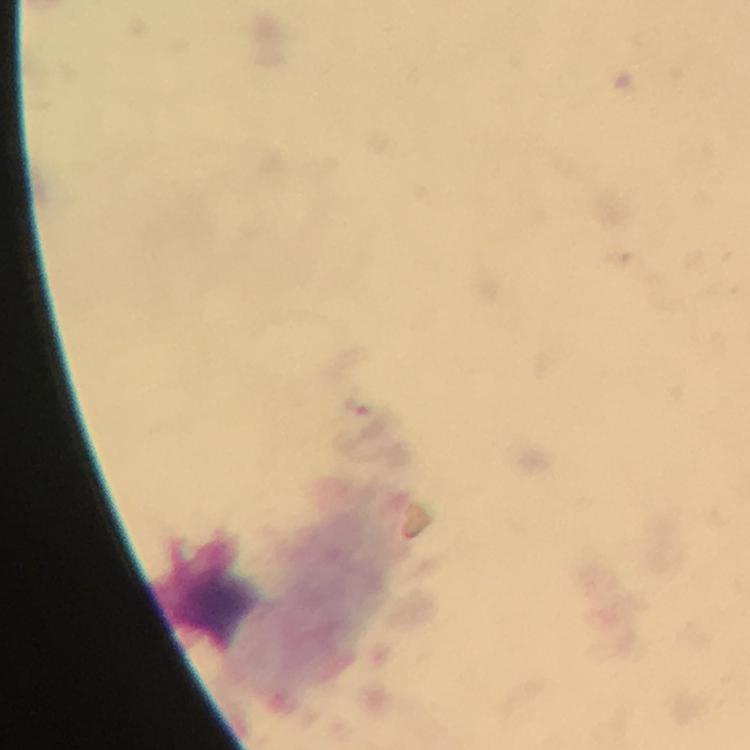

Approximate centers as {x, y} in pixels.
Summary:
  - Leukocyte locations: {214, 586}
  - Stain: Giemsa
  - Preparation: thick smear
  - Malaria parasites: none seen
  - Capture: smartphone camera through the microscope
  - Image size: 750×750 pixels
  - Cropped from: one field of view
  - Immersion oil: applied
  - Magnification: 100x
  - Context: from a malaria diagnostic workup